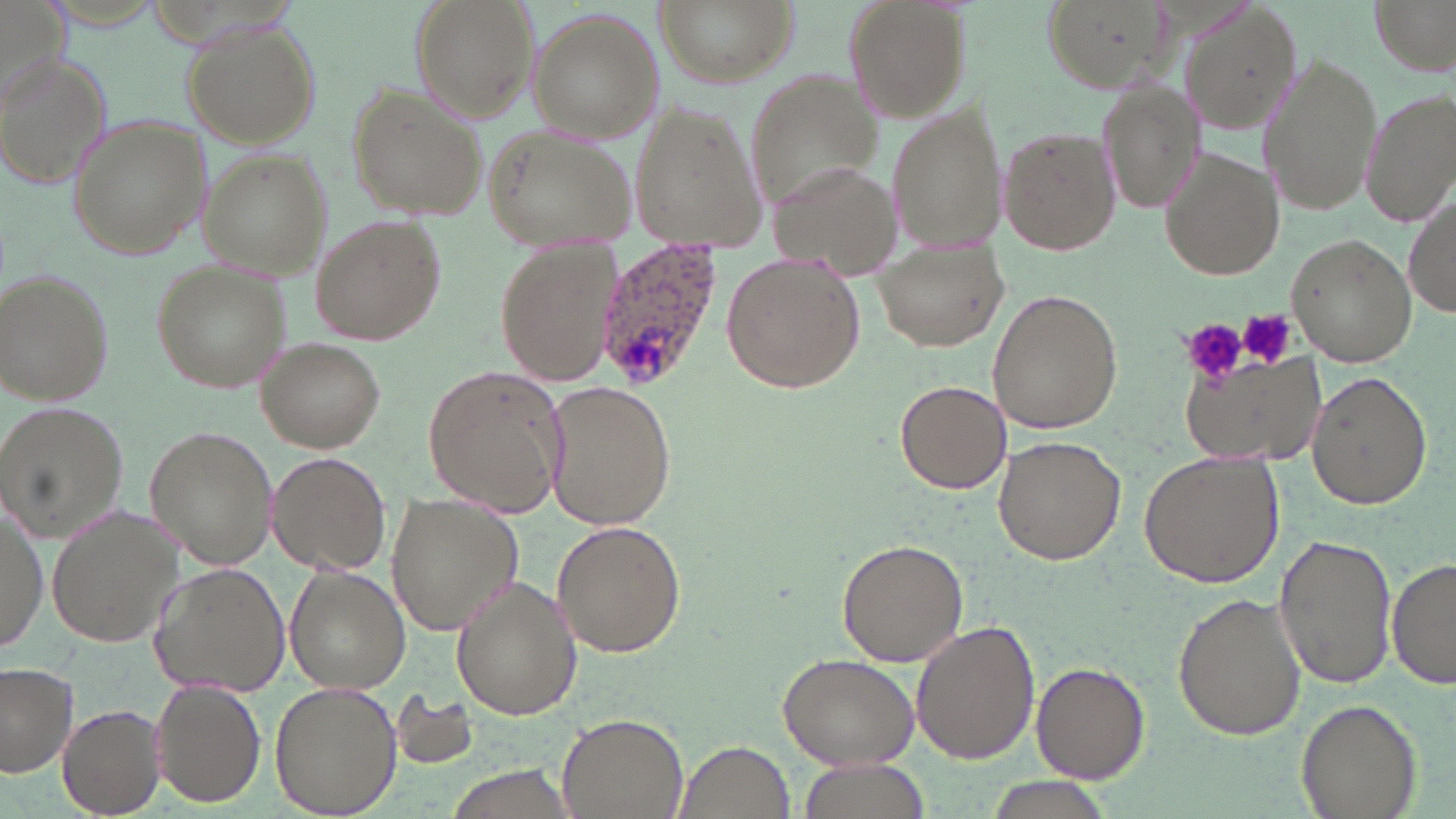
Plasmodium ovale-infected red blood cell locations = approximate bounding boxes as (x1, y1, x2, y2) in pixels: (592, 243, 723, 392)
slide-level diagnosis = Plasmodium ovale
field of view = one of a larger specimen
image size = 1456×819 pixels
stain = May-Grünwald-Giemsa
magnification = 1000x
uninfected red blood cell locations = approximate bounding boxes as (x1, y1, x2, y2) in pixels: (412, 0, 536, 120), (652, 0, 797, 88), (842, 0, 973, 126), (1370, 0, 1454, 74), (1043, 1, 1191, 97), (1172, 5, 1304, 136), (524, 6, 663, 143), (183, 19, 321, 147), (0, 52, 111, 189), (1259, 56, 1383, 218), (742, 68, 885, 215), (1099, 81, 1203, 211), (346, 84, 485, 223), (1359, 88, 1456, 227), (886, 100, 1007, 254), (628, 101, 773, 249), (65, 113, 210, 261), (481, 123, 637, 252), (1000, 126, 1120, 256), (197, 150, 333, 278), (1161, 150, 1283, 281), (766, 161, 899, 272), (1405, 189, 1455, 321), (311, 215, 445, 343), (1287, 234, 1419, 366), (492, 236, 623, 388), (874, 247, 1008, 351), (722, 252, 866, 394), (151, 260, 291, 395), (1, 269, 115, 406), (988, 290, 1122, 435), (256, 338, 384, 453), (1184, 360, 1325, 466), (424, 365, 567, 516), (1307, 370, 1432, 510), (895, 380, 1010, 495), (545, 382, 676, 530), (0, 399, 128, 542), (145, 426, 277, 568), (994, 436, 1127, 566), (1138, 448, 1285, 587), (267, 452, 391, 577), (385, 495, 523, 635), (0, 503, 44, 649), (47, 506, 187, 647), (550, 522, 686, 658), (1275, 534, 1395, 690), (838, 539, 967, 667), (1387, 558, 1456, 690), (151, 563, 291, 695), (284, 566, 410, 694), (450, 575, 584, 721), (1173, 592, 1307, 741), (910, 620, 1041, 766), (778, 649, 919, 769), (1031, 662, 1149, 783), (0, 663, 77, 777), (149, 679, 266, 808), (269, 682, 402, 816), (390, 693, 482, 771), (1295, 698, 1420, 819), (59, 703, 167, 817), (556, 712, 688, 817), (673, 740, 796, 819), (795, 757, 930, 819), (438, 763, 583, 819), (982, 781, 1107, 819)
preparation = thin blood smear
modality = optical microscopy
platelet locations = approximate bounding boxes as (x1, y1, x2, y2) in pixels: (1238, 309, 1297, 368), (1179, 317, 1248, 384)